Assess the morphology of the red blood cells.
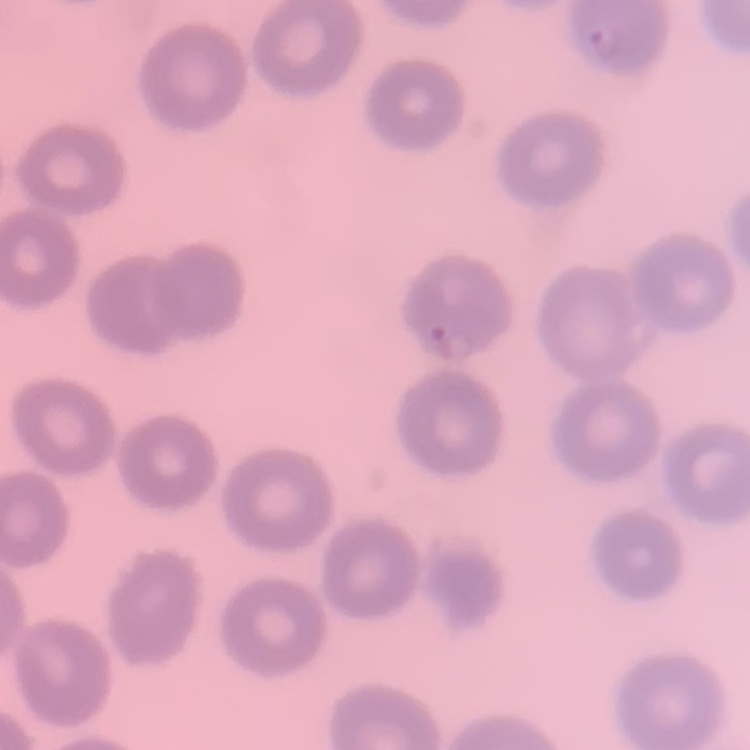
They show no rouleaux formation.

Summary:
  - Image type: square crop of a larger photomicrograph
  - Stain: Field's or Giemsa
  - Preparation: thin blood smear